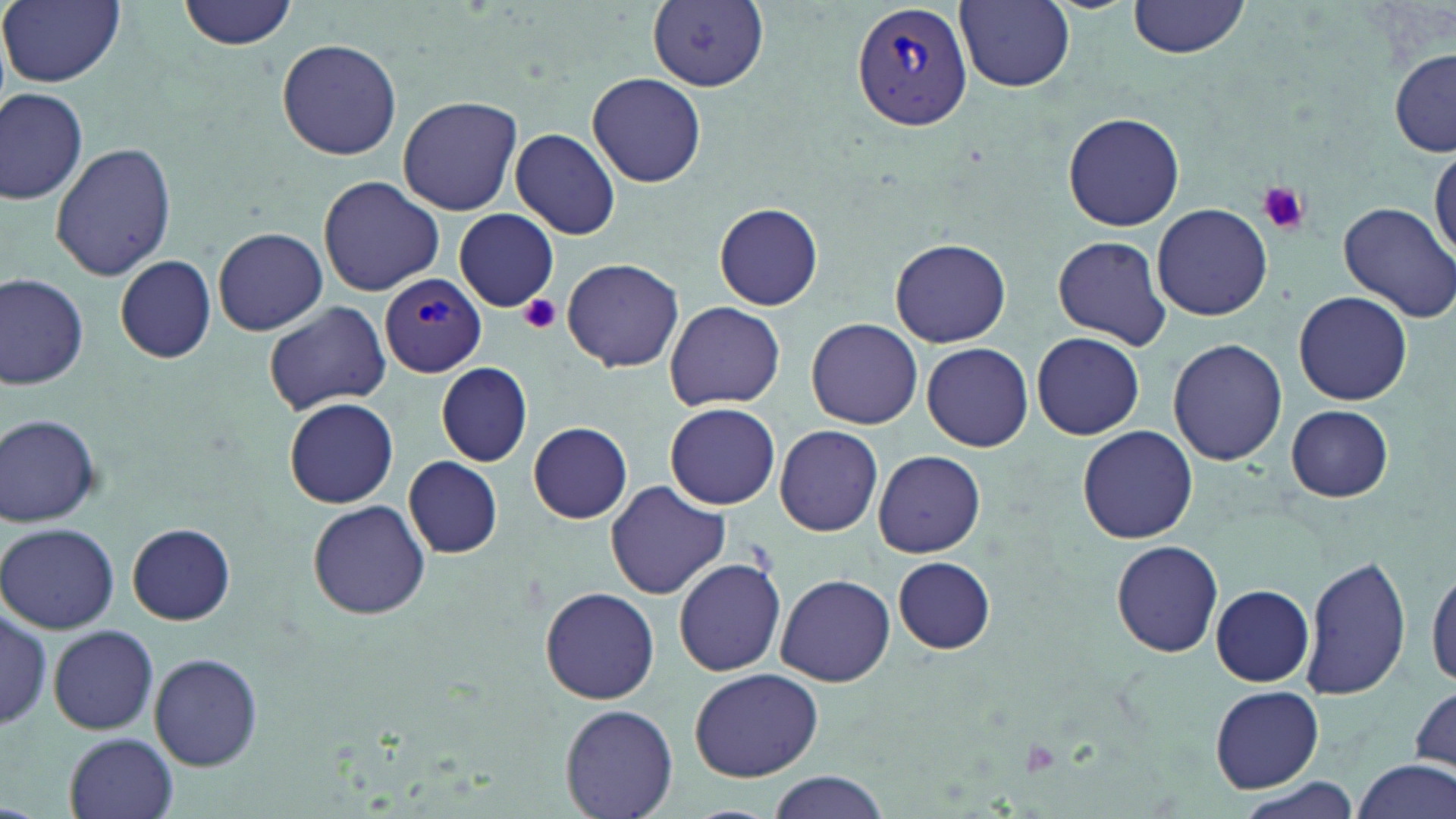

Summary:
  - Coordinate format: approximate bounding boxes as named x1/y1/x2/y2 corners in pixels
  - Plasmodium vivax-infected red blood cell locations: (x1=850, y1=1, x2=973, y2=134), (x1=380, y1=275, x2=486, y2=378)
  - Uninfected red blood cell locations: (x1=178, y1=0, x2=298, y2=50), (x1=1128, y1=0, x2=1248, y2=58), (x1=2, y1=1, x2=124, y2=88), (x1=648, y1=2, x2=770, y2=90), (x1=956, y1=2, x2=1075, y2=91), (x1=275, y1=38, x2=402, y2=160), (x1=1390, y1=50, x2=1455, y2=158), (x1=587, y1=71, x2=706, y2=188), (x1=0, y1=90, x2=89, y2=204), (x1=397, y1=96, x2=522, y2=215), (x1=1063, y1=111, x2=1185, y2=231), (x1=509, y1=128, x2=622, y2=240), (x1=50, y1=141, x2=178, y2=281), (x1=1431, y1=144, x2=1456, y2=261), (x1=317, y1=175, x2=446, y2=296), (x1=1337, y1=201, x2=1456, y2=321), (x1=714, y1=202, x2=823, y2=311), (x1=1152, y1=204, x2=1273, y2=320), (x1=453, y1=209, x2=558, y2=311), (x1=213, y1=226, x2=328, y2=335), (x1=1052, y1=236, x2=1172, y2=348), (x1=889, y1=238, x2=1011, y2=348), (x1=115, y1=255, x2=215, y2=364), (x1=562, y1=257, x2=684, y2=372), (x1=0, y1=275, x2=89, y2=388), (x1=1292, y1=290, x2=1413, y2=405), (x1=263, y1=300, x2=393, y2=413), (x1=665, y1=301, x2=786, y2=411), (x1=806, y1=318, x2=922, y2=428), (x1=1031, y1=331, x2=1145, y2=440), (x1=1167, y1=337, x2=1287, y2=466), (x1=920, y1=341, x2=1033, y2=451), (x1=435, y1=362, x2=532, y2=468), (x1=283, y1=397, x2=399, y2=508), (x1=665, y1=402, x2=780, y2=509), (x1=1286, y1=405, x2=1395, y2=502), (x1=0, y1=413, x2=103, y2=527), (x1=528, y1=421, x2=632, y2=524), (x1=774, y1=425, x2=882, y2=536), (x1=1077, y1=427, x2=1199, y2=544), (x1=874, y1=450, x2=986, y2=559), (x1=403, y1=455, x2=504, y2=558), (x1=605, y1=481, x2=731, y2=601), (x1=306, y1=499, x2=431, y2=619), (x1=1, y1=522, x2=118, y2=634), (x1=128, y1=522, x2=235, y2=624), (x1=1109, y1=539, x2=1224, y2=657), (x1=1300, y1=554, x2=1413, y2=701), (x1=674, y1=557, x2=787, y2=677), (x1=893, y1=557, x2=994, y2=654), (x1=1426, y1=562, x2=1456, y2=693), (x1=775, y1=575, x2=895, y2=686), (x1=540, y1=585, x2=660, y2=705), (x1=1210, y1=585, x2=1314, y2=686), (x1=0, y1=604, x2=54, y2=731), (x1=48, y1=624, x2=158, y2=735), (x1=150, y1=651, x2=264, y2=772), (x1=689, y1=667, x2=823, y2=782), (x1=1408, y1=679, x2=1456, y2=778), (x1=1210, y1=685, x2=1323, y2=791), (x1=561, y1=704, x2=677, y2=819), (x1=64, y1=733, x2=178, y2=819), (x1=1351, y1=761, x2=1455, y2=819), (x1=766, y1=773, x2=893, y2=819)
  - Platelet locations: (x1=1256, y1=183, x2=1309, y2=235), (x1=519, y1=294, x2=562, y2=333), (x1=1016, y1=737, x2=1064, y2=778)
  - Slide-level diagnosis: Plasmodium vivax
  - Preparation: thin blood smear
  - Modality: light microscopy
  - Image size: 1456×819 pixels
  - Magnification: 1000x
  - Stain: May-Grünwald-Giemsa
  - Field of view: one of a larger specimen